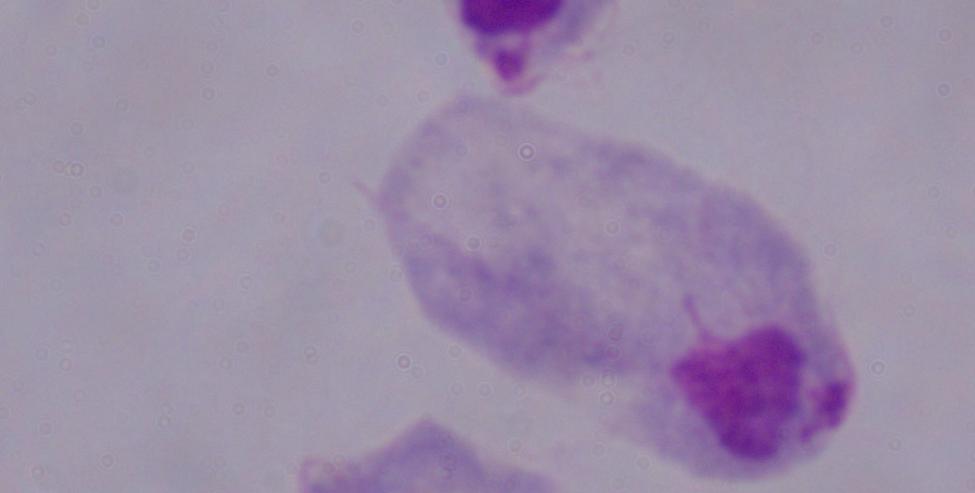

magnification = 1000x
modality = micrograph
identification = trichomonad